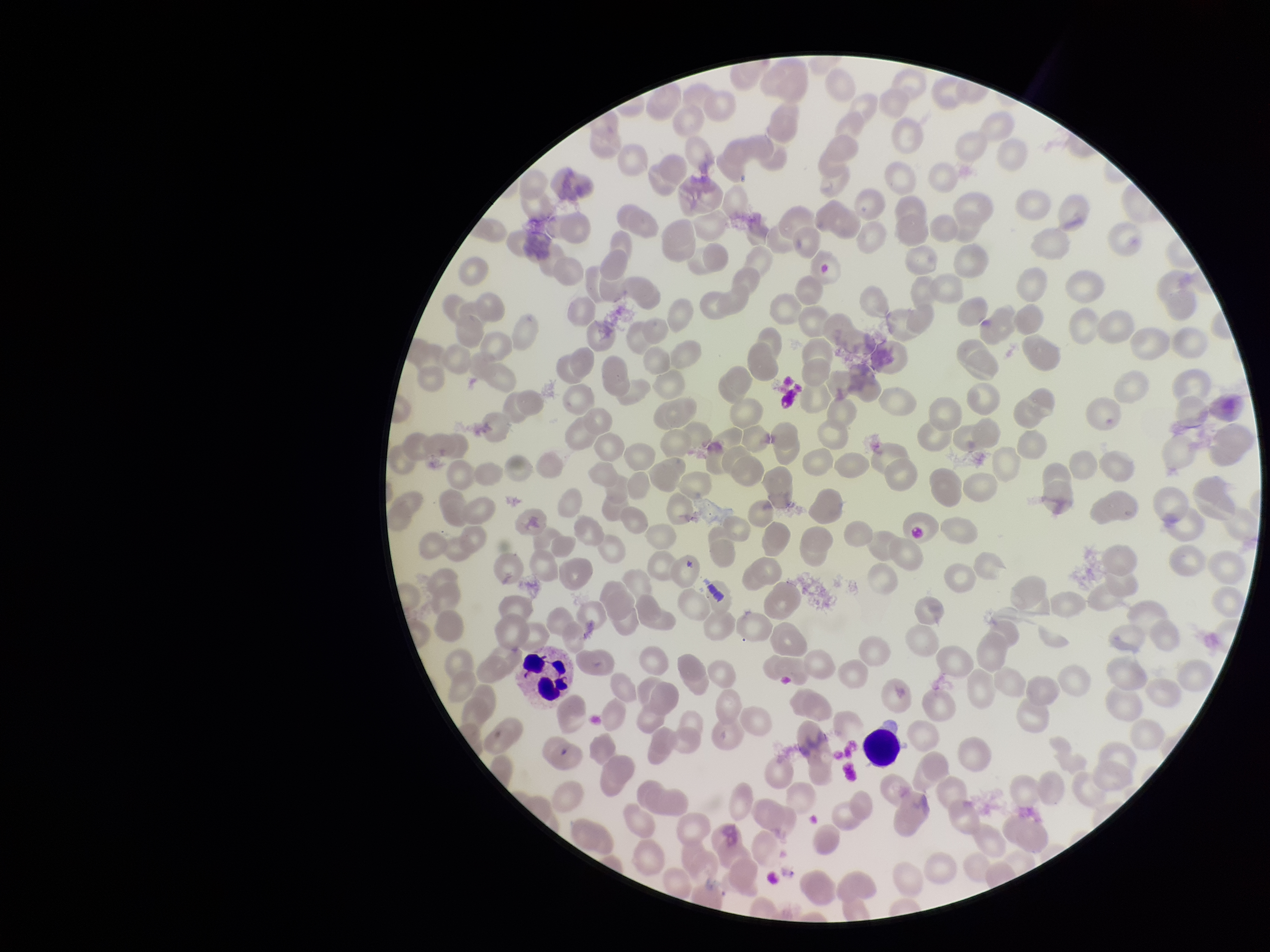 Patient malaria status: negative. Single field of view. Image is 1270×952 pixels. Photographed through the microscope eyepiece with a smartphone camera. Preparation: thin blood smear. Parasitized red blood cell count: 0. Stained with Giemsa. Red blood cell count: 227. Parasitized red blood cells: none identified.